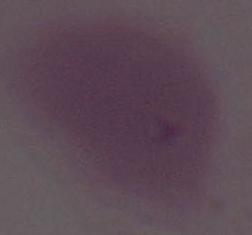 1000x magnification. Micrograph. A red blood cell is shown.